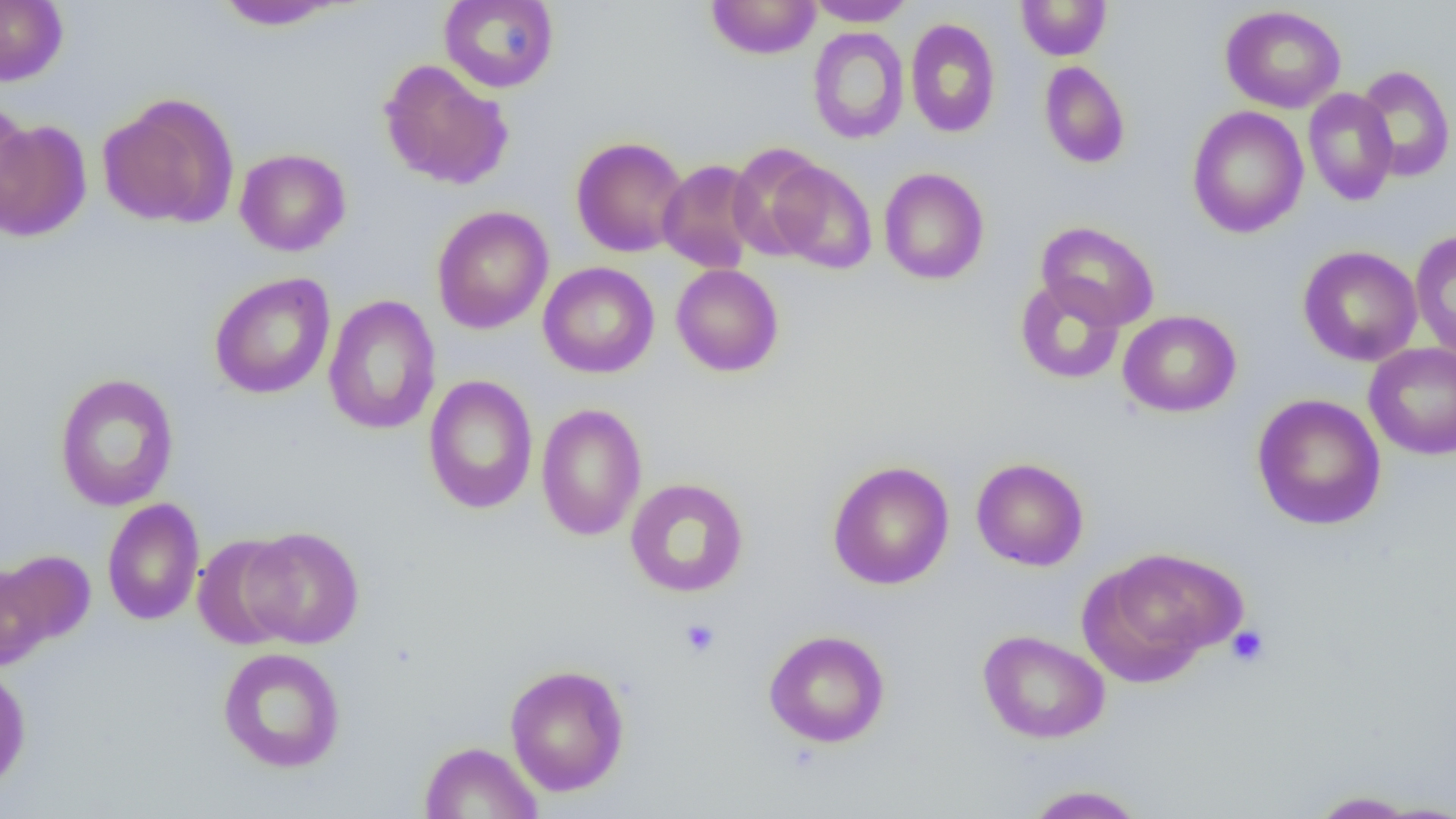

Approximate bounding boxes as (x1, y1, x2, y2) in pixels. Uninfected red blood cell locations: (0, 0, 68, 86), (439, 0, 559, 93), (706, 0, 821, 59), (805, 0, 916, 27), (1016, 0, 1112, 60), (213, 1, 345, 30), (1220, 5, 1346, 113), (905, 17, 1001, 138), (807, 27, 910, 144), (378, 59, 514, 190), (1039, 61, 1130, 168), (1355, 65, 1455, 182), (1303, 87, 1398, 205), (99, 93, 239, 230), (0, 98, 34, 229), (1187, 105, 1308, 238), (1, 119, 93, 242), (571, 136, 689, 258), (726, 142, 829, 260), (234, 148, 351, 256), (657, 159, 763, 274), (769, 161, 877, 274), (878, 167, 989, 285), (431, 206, 554, 334), (1035, 221, 1160, 331), (1409, 229, 1456, 361), (1297, 245, 1423, 367), (538, 262, 660, 379), (670, 263, 784, 377), (209, 272, 336, 399), (1014, 277, 1126, 385), (322, 294, 442, 435), (1118, 310, 1241, 417), (1364, 342, 1456, 460), (54, 373, 179, 511), (423, 374, 538, 515), (1252, 394, 1386, 530), (535, 402, 648, 541), (972, 457, 1089, 571), (827, 460, 955, 590), (625, 478, 749, 598), (102, 498, 205, 626), (241, 525, 364, 649), (192, 533, 300, 650), (1083, 546, 1247, 679), (1, 549, 96, 647), (1, 563, 52, 671), (763, 629, 890, 748), (977, 629, 1110, 744), (217, 647, 346, 772), (504, 664, 630, 796), (0, 666, 32, 795), (419, 741, 542, 818), (1021, 784, 1149, 818), (1305, 790, 1427, 817). Platelet locations: (679, 618, 721, 658), (1226, 624, 1271, 668). Slide-level diagnosis: negative for blood parasites. Image is 1456×819 pixels. Single field of view. Optical microscopy. Thin blood smear. 1000x magnification.